Identify the parasite.
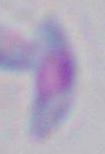
This is Toxoplasma gondii.

{
  "modality": "micrograph",
  "magnification": "1000x"
}